Name the cell type shown.
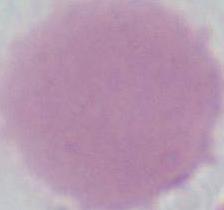

An erythrocyte.

Photomicrograph. 1000x magnification.